Assess the morphology of the red blood cells.
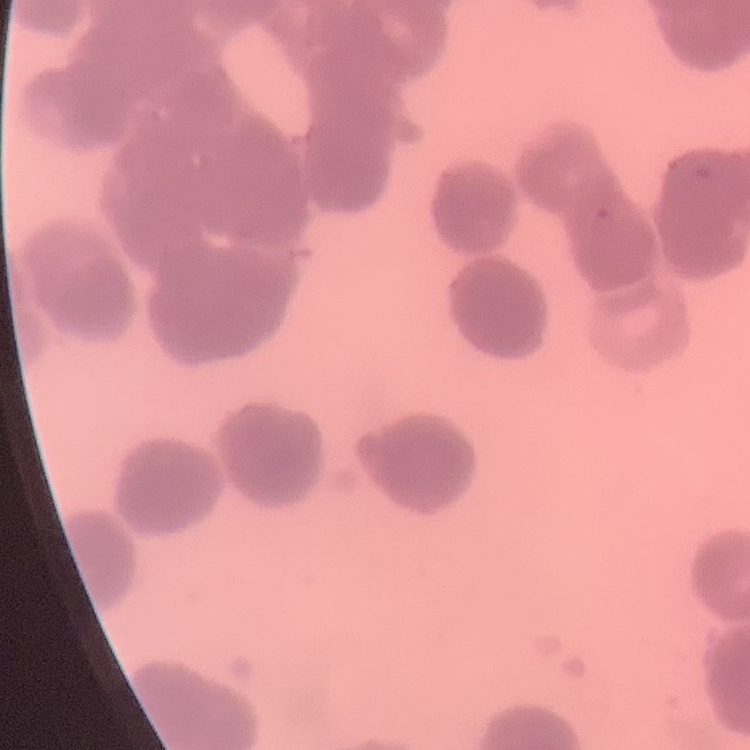

They show rouleaux formation.

Field's or Giemsa stain. Thin blood film. One tile cut from a larger photomicrograph.